Report the malaria status of this cell.
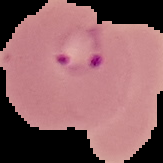

It is parasitized.

Image is 163×163 pixels. From a thin blood smear. Segmented cell region on a black background.